Give the position of every leukocyte visible.
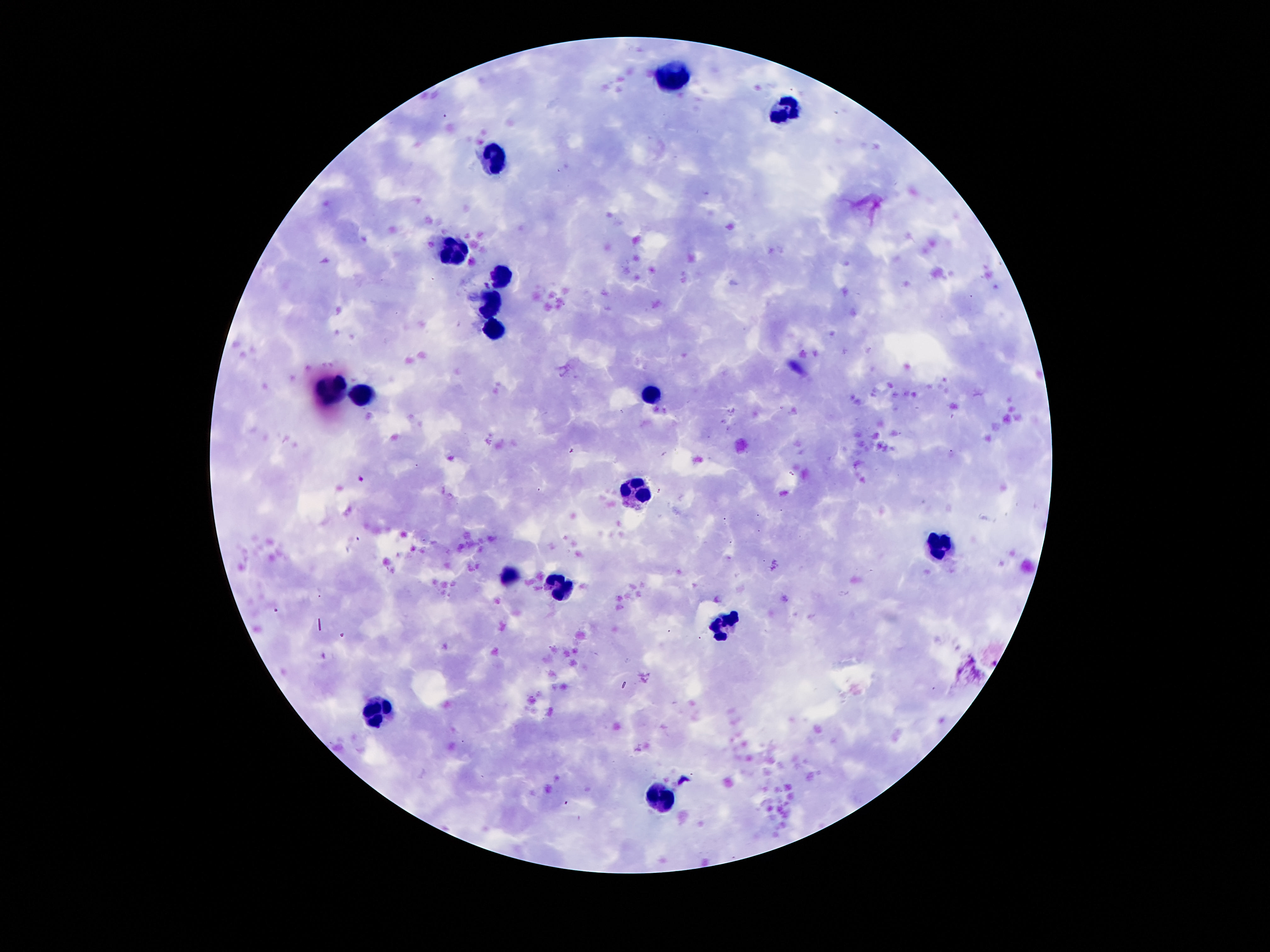

Approximate centers as {x, y} in pixels.
Leukocytes: {674, 78}, {787, 110}, {496, 157}, {453, 250}, {503, 275}, {492, 300}, {496, 330}, {651, 391}, {331, 393}, {360, 398}, {639, 491}, {941, 545}, {510, 579}, {560, 588}, {726, 620}, {381, 713}, {658, 799}.

magnification: 100x
preparation: thick blood smear
capture: smartphone camera through the microscope eyepiece
stain: Giemsa
image_size: 1270×952 pixels
field_of_view: single
patient_malaria_status: not infected